Report the malaria status.
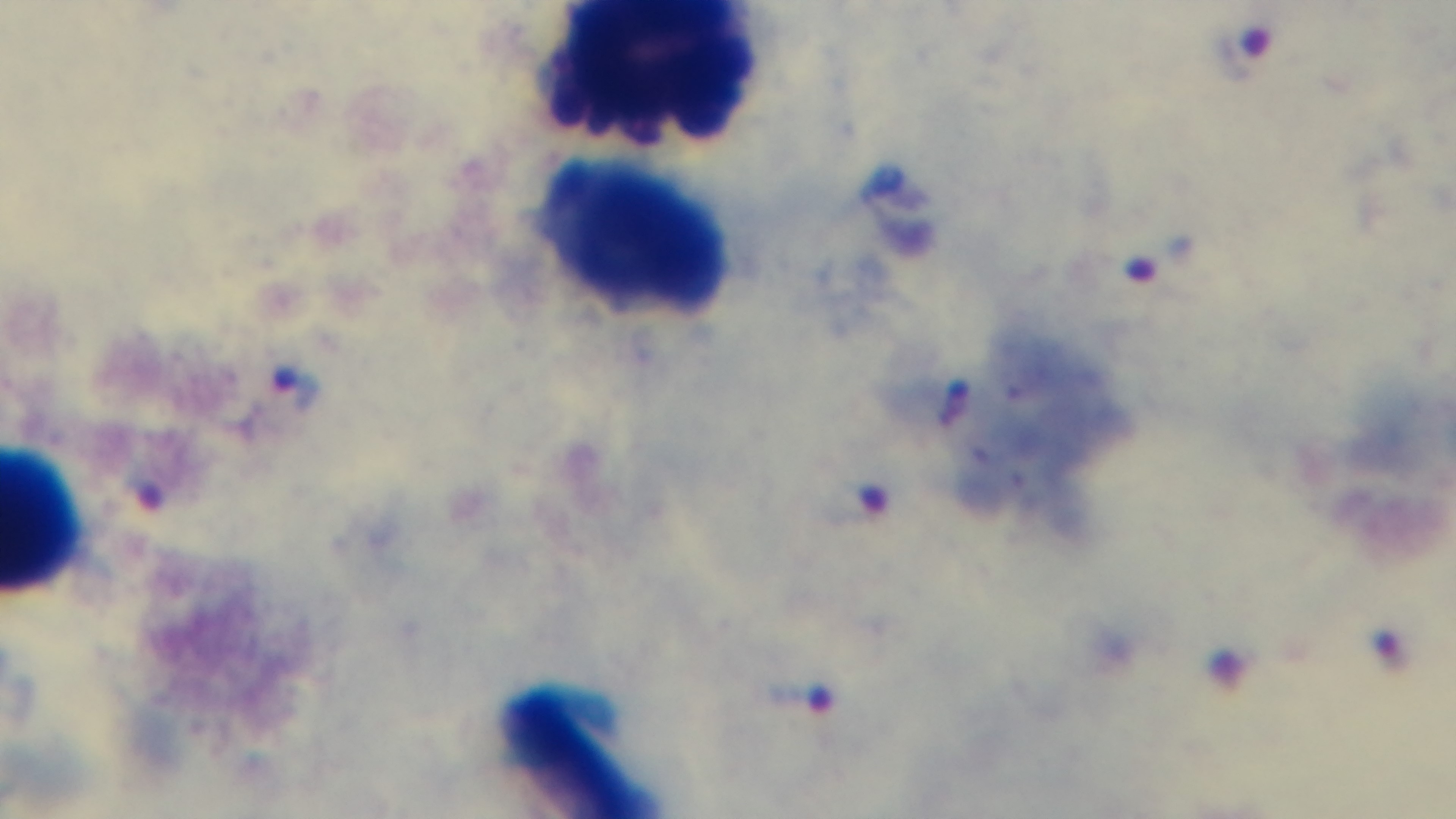

It is infected.

capture: mounted 4K digital camera
objective: 100x oil immersion
preparation: thick smear
modality: light microscopy
field_of_view: one from the slide
stain: Giemsa